Identify the preparation type.
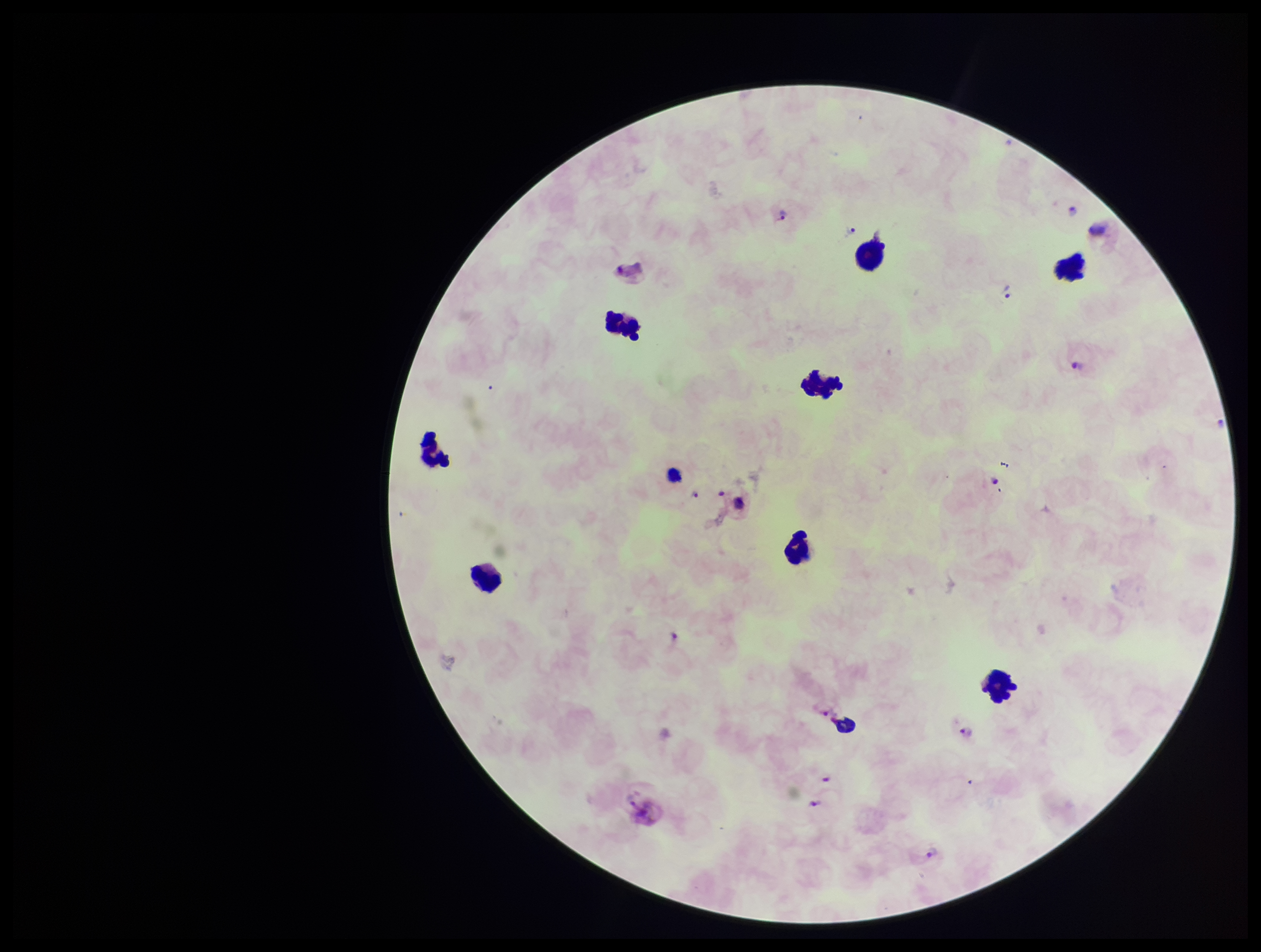
A thick smear.

Single field of view. Plasmodium parasites: detected. Smartphone photograph taken through the eyepiece of a microscope. Leukocyte count: 8. Species reported for this patient: Plasmodium vivax. Stained with Giemsa. Patient malaria status: positive. Parasite count: 10. Image is 1261×952 pixels.